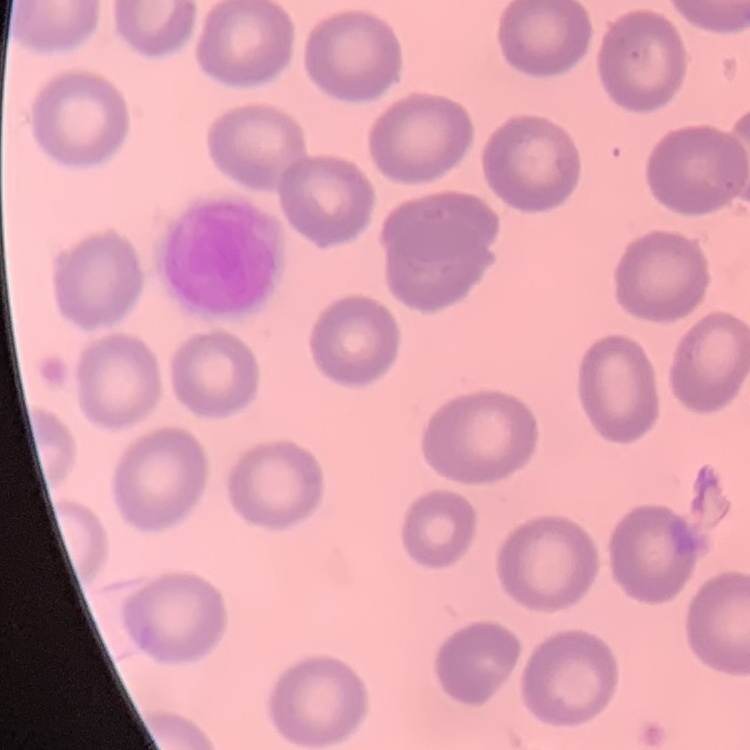

erythrocyte morphology = no rouleaux formation
image type = square crop of a larger photomicrograph
preparation = thin blood film
stain = Field's or Giemsa